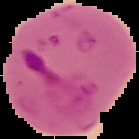
{
  "image_size": "139×139 pixels",
  "image_type": "cell region segmented out of the field of view; surrounding area masked to black",
  "preparation": "thin blood film",
  "result": "Plasmodium parasites detected"
}